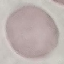

Summary:
  - Malaria status: uninfected
  - Stain: Giemsa
  - Image type: automatically extracted cell patch, resized to 64 × 64 pixels
  - Preparation: thin blood film
  - Capture: smartphone camera at the microscope eyepiece